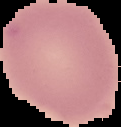 The area outside the segmented cell region is set to black. Result: no Plasmodium parasites detected. Image is 121×127 pixels. From a thin blood smear.